Locate and identify every blood parasite.
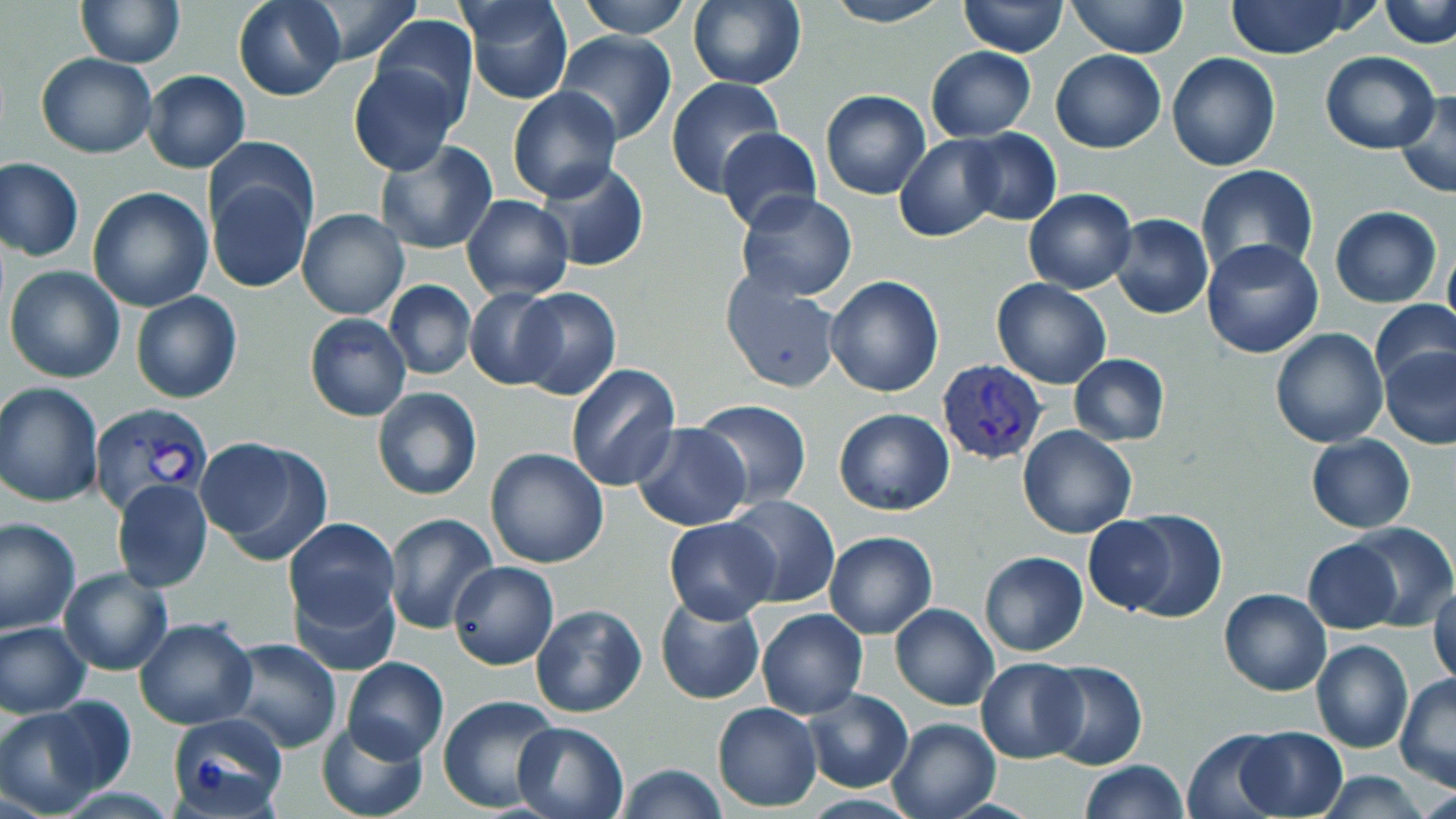

Approximate bounding boxes as named x1/y1/x2/y2 corners in pixels.
Plasmodium vivax-infected red blood cells: (x1=938, y1=360, x2=1046, y2=464), (x1=89, y1=402, x2=215, y2=516).
No Plasmodium falciparum, Plasmodium ovale, Plasmodium malariae, Babesia divergens, or Trypanosoma brucei observed.

{
  "slide_level_diagnosis": "Plasmodium vivax",
  "stain": "May-Grünwald-Giemsa",
  "field_of_view": "single",
  "modality": "optical microscopy",
  "magnification": "1000x",
  "uninfected_red_blood_cell_locations": "approximate bounding boxes as named x1/y1/x2/y2 corners in pixels: (x1=76, y1=0, x2=183, y2=67), (x1=233, y1=0, x2=345, y2=101), (x1=292, y1=0, x2=425, y2=66), (x1=462, y1=0, x2=575, y2=106), (x1=576, y1=0, x2=691, y2=38), (x1=686, y1=0, x2=806, y2=89), (x1=821, y1=0, x2=949, y2=27), (x1=1222, y1=0, x2=1365, y2=59), (x1=1381, y1=0, x2=1456, y2=49), (x1=1067, y1=1, x2=1188, y2=57), (x1=959, y1=2, x2=1068, y2=56), (x1=370, y1=16, x2=477, y2=123), (x1=550, y1=33, x2=677, y2=147), (x1=925, y1=47, x2=1036, y2=142), (x1=1051, y1=49, x2=1166, y2=154), (x1=1167, y1=51, x2=1281, y2=170), (x1=1320, y1=51, x2=1441, y2=153), (x1=36, y1=53, x2=158, y2=159), (x1=347, y1=63, x2=462, y2=177), (x1=143, y1=70, x2=250, y2=174), (x1=665, y1=76, x2=783, y2=197), (x1=507, y1=86, x2=624, y2=203), (x1=821, y1=90, x2=931, y2=200), (x1=1395, y1=90, x2=1456, y2=199), (x1=715, y1=128, x2=822, y2=233), (x1=959, y1=128, x2=1061, y2=226), (x1=896, y1=134, x2=1004, y2=241), (x1=204, y1=138, x2=318, y2=243), (x1=373, y1=140, x2=496, y2=254), (x1=1, y1=158, x2=85, y2=262), (x1=531, y1=159, x2=649, y2=272), (x1=1195, y1=165, x2=1320, y2=282), (x1=206, y1=172, x2=313, y2=293), (x1=87, y1=187, x2=214, y2=313), (x1=1022, y1=187, x2=1138, y2=295), (x1=735, y1=192, x2=858, y2=302), (x1=462, y1=195, x2=573, y2=300), (x1=1331, y1=206, x2=1441, y2=308), (x1=296, y1=208, x2=409, y2=320), (x1=1110, y1=215, x2=1213, y2=319), (x1=1199, y1=238, x2=1324, y2=359), (x1=1442, y1=239, x2=1456, y2=343), (x1=5, y1=265, x2=126, y2=383), (x1=721, y1=274, x2=844, y2=393), (x1=823, y1=275, x2=945, y2=397), (x1=990, y1=277, x2=1111, y2=389), (x1=383, y1=280, x2=476, y2=380), (x1=464, y1=288, x2=565, y2=389), (x1=510, y1=288, x2=621, y2=399), (x1=131, y1=291, x2=242, y2=404), (x1=1370, y1=299, x2=1456, y2=393), (x1=531, y1=310, x2=650, y2=464), (x1=304, y1=314, x2=411, y2=421), (x1=1269, y1=328, x2=1390, y2=447), (x1=1378, y1=344, x2=1456, y2=449), (x1=1069, y1=353, x2=1170, y2=447), (x1=566, y1=364, x2=681, y2=491), (x1=0, y1=383, x2=104, y2=507), (x1=371, y1=387, x2=482, y2=501), (x1=693, y1=400, x2=810, y2=508), (x1=834, y1=407, x2=954, y2=516), (x1=630, y1=422, x2=753, y2=532), (x1=1017, y1=424, x2=1138, y2=538), (x1=1306, y1=433, x2=1415, y2=532), (x1=196, y1=438, x2=334, y2=565), (x1=484, y1=448, x2=610, y2=569), (x1=111, y1=478, x2=214, y2=592), (x1=723, y1=494, x2=840, y2=608), (x1=1115, y1=510, x2=1228, y2=623), (x1=382, y1=512, x2=499, y2=635), (x1=1083, y1=515, x2=1179, y2=615), (x1=281, y1=516, x2=400, y2=639), (x1=663, y1=516, x2=780, y2=624), (x1=0, y1=517, x2=82, y2=634), (x1=1342, y1=523, x2=1455, y2=630), (x1=824, y1=530, x2=937, y2=638), (x1=1303, y1=539, x2=1400, y2=633), (x1=978, y1=550, x2=1089, y2=657), (x1=449, y1=561, x2=559, y2=669), (x1=58, y1=567, x2=174, y2=676), (x1=290, y1=573, x2=401, y2=675), (x1=1429, y1=579, x2=1455, y2=691), (x1=1219, y1=588, x2=1332, y2=696), (x1=655, y1=596, x2=766, y2=705), (x1=530, y1=603, x2=648, y2=717), (x1=889, y1=604, x2=999, y2=710), (x1=756, y1=607, x2=867, y2=719), (x1=134, y1=618, x2=256, y2=731), (x1=1, y1=621, x2=92, y2=718), (x1=221, y1=638, x2=342, y2=754), (x1=1311, y1=639, x2=1414, y2=753), (x1=342, y1=656, x2=449, y2=763), (x1=976, y1=657, x2=1085, y2=763), (x1=1041, y1=660, x2=1147, y2=770), (x1=1395, y1=673, x2=1456, y2=788), (x1=801, y1=688, x2=913, y2=793), (x1=438, y1=695, x2=564, y2=815), (x1=712, y1=702, x2=822, y2=811), (x1=0, y1=703, x2=113, y2=814), (x1=167, y1=711, x2=289, y2=816), (x1=317, y1=717, x2=430, y2=819), (x1=885, y1=718, x2=1000, y2=819), (x1=511, y1=719, x2=629, y2=819), (x1=1234, y1=726, x2=1347, y2=818), (x1=1183, y1=728, x2=1286, y2=818), (x1=1079, y1=759, x2=1188, y2=818), (x1=613, y1=763, x2=728, y2=819), (x1=1314, y1=770, x2=1433, y2=818)",
  "image_size": "1456×819 pixels",
  "preparation": "thin blood film"
}